Point out Plasmodium parasites and leukocytes.
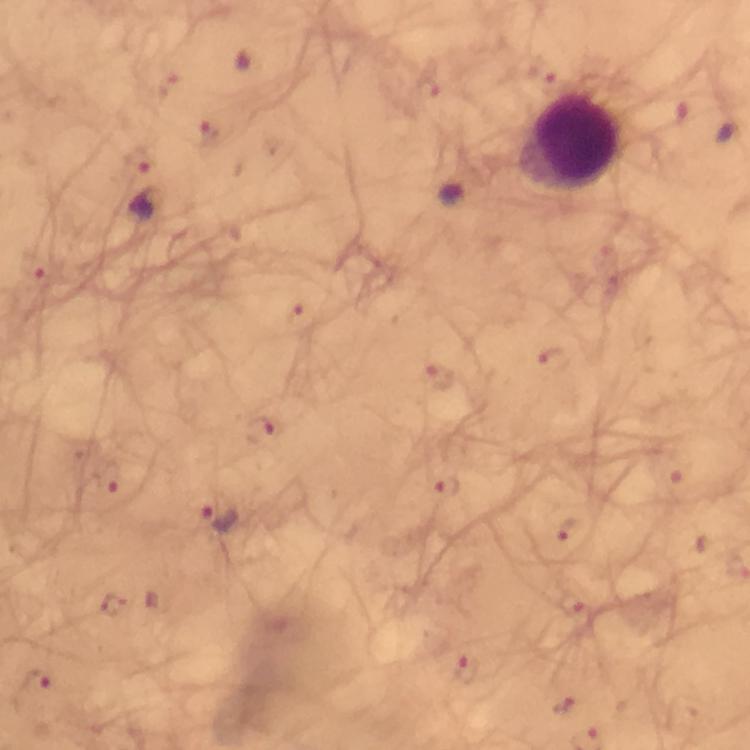
Approximate centers as (x, y) in pixels.
Plasmodium parasites: (550, 76), (427, 87), (166, 92), (209, 133), (136, 159), (453, 191), (35, 264), (298, 318), (552, 360), (440, 378), (259, 431), (668, 471), (111, 480), (444, 485), (222, 516), (571, 531), (573, 604), (112, 606), (464, 672), (35, 684), (564, 706).
Leukocytes: (568, 144).

Summary:
  - Stain: Giemsa
  - Immersion oil: applied
  - Cropped from: a single field of view
  - Context: from a diagnostic examination for malaria
  - Capture: smartphone camera through the microscope
  - Magnification: 100x
  - Image size: 750×750 pixels
  - Preparation: thick smear